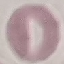
Result: no malaria parasites seen. Photographed with a smartphone camera at the microscope eyepiece. Thin smear of blood. Cell patch, automatically extracted from a larger field of view and resized to 64 × 64 pixels. Giemsa stain.